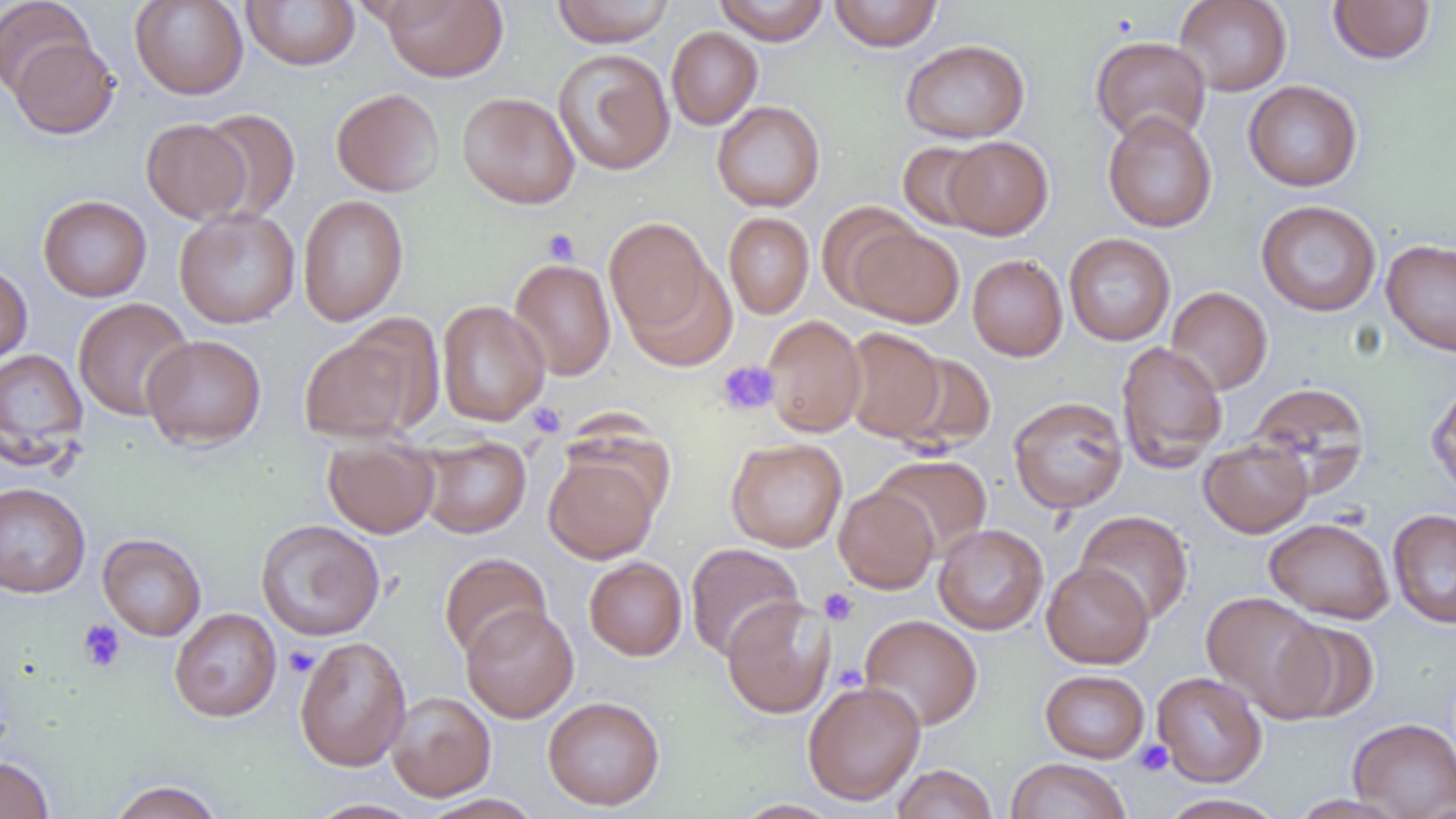
Summary:
  - Coordinate format: approximate bounding boxes as (x1,y1)-(x2,y2) corner pairs in pixels
  - Uninfected red blood cell locations: (0,0)-(96,98), (130,0)-(248,100), (241,0)-(360,70), (381,0)-(508,82), (552,0)-(674,47), (714,0)-(828,45), (828,0)-(943,51), (1174,0)-(1292,96), (1328,0)-(1436,64), (666,26)-(763,129), (9,36)-(119,139), (1090,36)-(1212,144), (900,38)-(1030,143), (553,48)-(675,176), (1243,80)-(1363,191), (331,88)-(445,197), (457,91)-(580,209), (712,101)-(825,212), (197,108)-(300,221), (1102,111)-(1218,233), (141,118)-(250,224), (942,135)-(1053,240), (897,140)-(994,232), (297,194)-(409,326), (37,195)-(152,302), (1256,200)-(1382,317), (816,201)-(922,307), (173,207)-(300,329), (723,212)-(814,319), (604,216)-(716,340), (847,226)-(964,328), (1064,233)-(1176,345), (1381,239)-(1456,356), (967,254)-(1068,361), (509,258)-(616,381), (621,259)-(738,371), (0,263)-(32,365), (1165,286)-(1273,395), (73,297)-(195,421), (436,299)-(549,426), (761,314)-(867,438), (841,328)-(945,442), (298,332)-(423,443), (141,334)-(267,450), (1115,341)-(1229,472), (0,347)-(88,463), (892,352)-(997,454), (1427,379)-(1456,498), (1248,382)-(1371,494), (1008,396)-(1129,514), (417,434)-(531,538), (322,436)-(439,539), (726,437)-(848,552), (1199,437)-(1313,538), (544,449)-(662,564), (872,454)-(991,559), (0,482)-(91,598), (834,486)-(939,594), (1388,508)-(1456,628), (1075,510)-(1193,624), (1264,518)-(1395,624), (256,519)-(385,641), (933,523)-(1048,635), (97,533)-(206,640), (685,543)-(805,661), (439,552)-(551,661), (584,556)-(687,660), (1041,561)-(1154,669), (1202,591)-(1331,720), (721,596)-(835,718), (461,604)-(579,722), (169,607)-(282,722), (859,614)-(983,731), (1274,619)-(1380,723), (294,636)-(412,772), (1040,669)-(1149,763), (1152,672)-(1267,787), (802,680)-(926,805), (387,691)-(496,802), (543,695)-(665,811), (1348,718)-(1456,818), (0,755)-(54,819), (1004,758)-(1131,819), (892,763)-(998,819), (107,780)-(225,819), (1159,793)-(1287,818), (419,794)-(544,819), (1286,794)-(1412,819), (307,798)-(426,818), (732,800)-(843,819)
  - Platelet locations: (542,229)-(580,264), (716,360)-(780,417), (525,403)-(566,438), (819,588)-(858,625), (77,619)-(126,672), (283,645)-(319,678), (1135,740)-(1174,776)
  - Slide-level diagnosis: negative for blood parasites
  - Magnification: 1000x
  - Field of view: single
  - Preparation: thin blood film
  - Modality: light microscopy
  - Image size: 1456×819 pixels